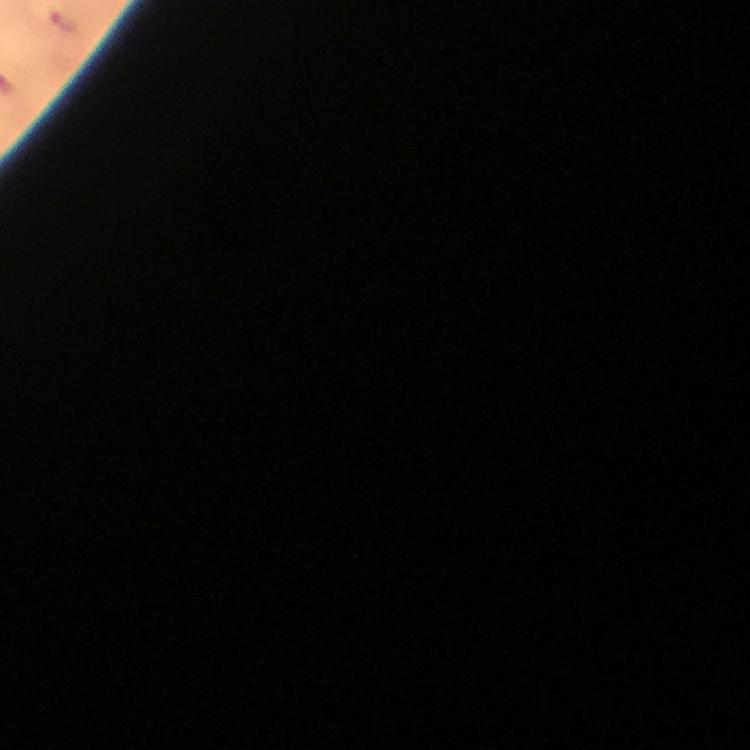
Approximate centers as [x, y] in pixels. Malaria parasite locations: [65, 21]. From a diagnostic examination for malaria. Image is 750×750 pixels. 100x magnification. Giemsa-stained preparation. Photographed with a smartphone mounted on the microscope. Thick smear. A crop from one field of view. Immersion oil applied.